Assess this cell for malaria.
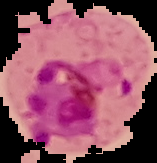

It is parasitized.

{
  "preparation": "thin blood film",
  "image_size": "157×163 pixels",
  "image_type": "segmented cell region on a black background"
}